Assess the morphology of the red blood cells.
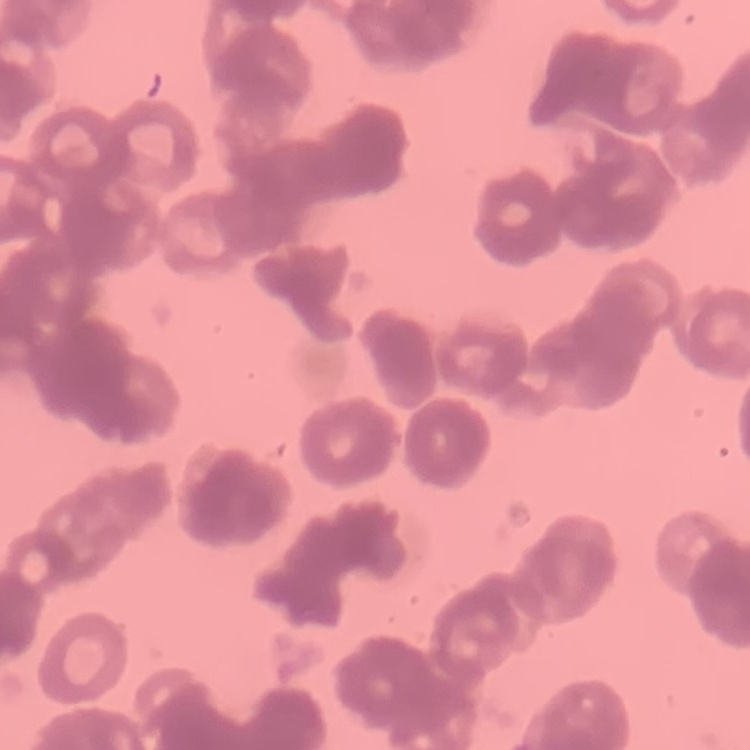
They show rouleaux formation.

Summary:
  - Image type: square crop of a larger photomicrograph
  - Stain: Field's or Giemsa
  - Preparation: thin blood smear